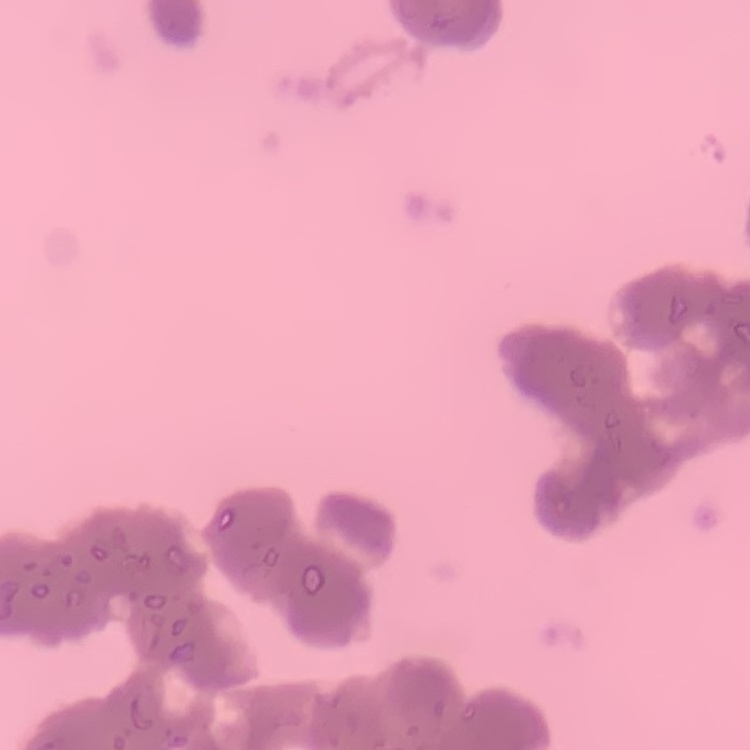 The erythrocytes show rouleaux formation. Field's or Giemsa stain. Square crop of a larger photomicrograph. Thin blood smear.